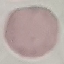
{
  "malaria_status": "uninfected",
  "stain": "Giemsa",
  "capture": "smartphone through the microscope eyepiece",
  "preparation": "thin blood film",
  "image_type": "cell patch, automatically extracted from a larger field of view and resized to 64 × 64 pixels"
}